Classify this cell by malaria status.
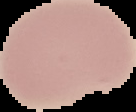

Uninfected.

Summary:
  - Preparation: thin blood film
  - Image type: cell region segmented out of the field of view; surrounding area masked to black
  - Image size: 136×112 pixels